State the blood parasite species.
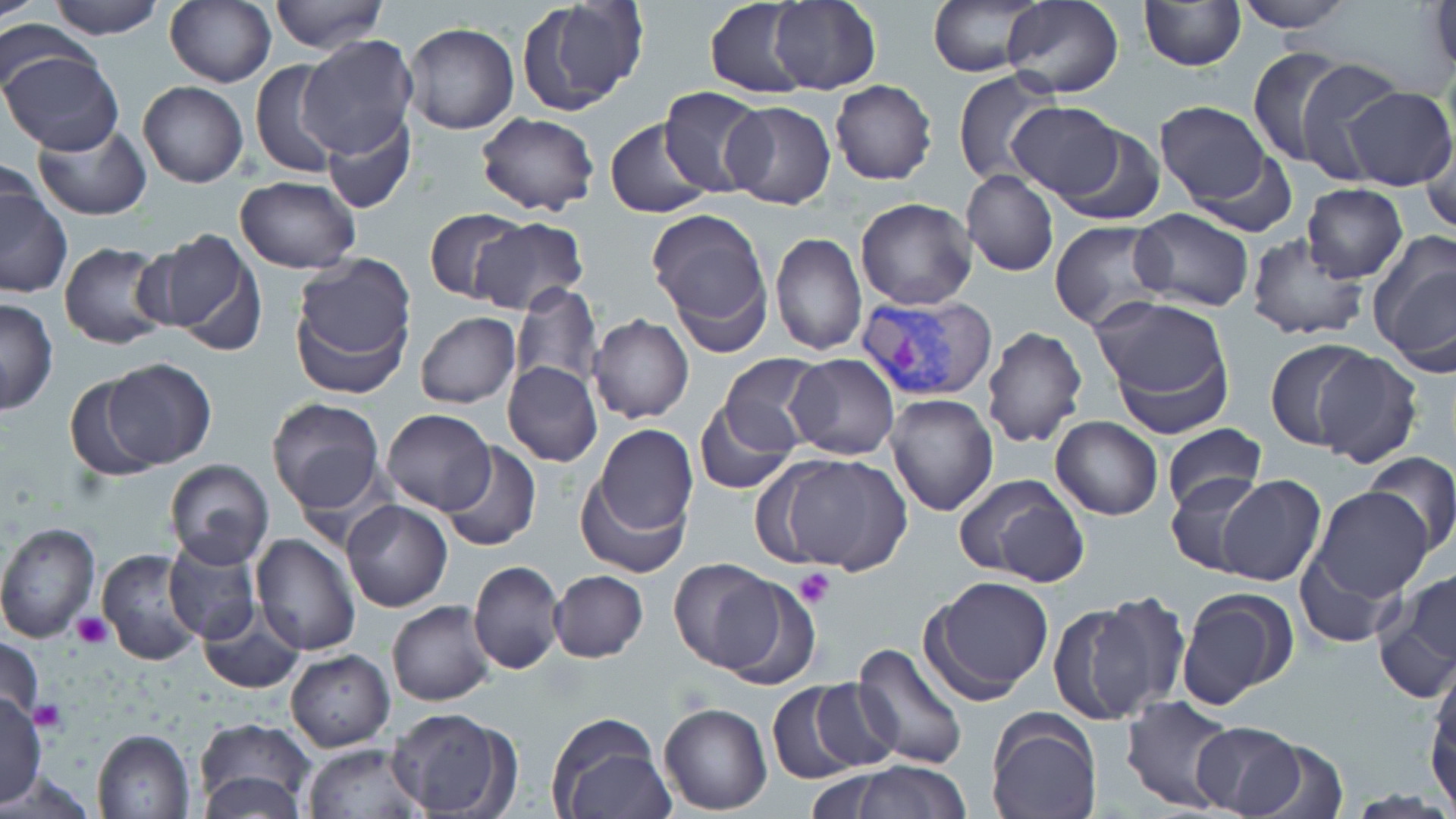
Plasmodium vivax.

preparation = thin blood film
platelet locations = approximate bounding boxes as named x1/y1/x2/y2 corners in pixels: (x1=795, y1=568, x2=835, y2=608), (x1=72, y1=611, x2=113, y2=651), (x1=31, y1=699, x2=65, y2=733)
modality = optical microscopy
image size = 1456×819 pixels
stain = May-Grünwald-Giemsa
Plasmodium vivax-infected red blood cell locations = approximate bounding boxes as named x1/y1/x2/y2 corners in pixels: (x1=855, y1=290, x2=998, y2=399)
field of view = one of a larger specimen
uninfected red blood cell locations = approximate bounding boxes as named x1/y1/x2/y2 corners in pixels: (x1=0, y1=0, x2=39, y2=22), (x1=48, y1=0, x2=165, y2=40), (x1=166, y1=0, x2=277, y2=87), (x1=268, y1=0, x2=387, y2=53), (x1=926, y1=0, x2=1047, y2=77), (x1=1232, y1=0, x2=1355, y2=32), (x1=516, y1=1, x2=649, y2=114), (x1=704, y1=1, x2=814, y2=98), (x1=768, y1=1, x2=881, y2=92), (x1=1002, y1=1, x2=1125, y2=98), (x1=1139, y1=1, x2=1247, y2=71), (x1=1425, y1=1, x2=1455, y2=83), (x1=0, y1=21, x2=89, y2=103), (x1=404, y1=22, x2=519, y2=135), (x1=297, y1=34, x2=418, y2=160), (x1=1246, y1=46, x2=1355, y2=168), (x1=1, y1=48, x2=123, y2=155), (x1=250, y1=59, x2=346, y2=176), (x1=1293, y1=60, x2=1408, y2=184), (x1=953, y1=71, x2=1062, y2=186), (x1=137, y1=80, x2=248, y2=187), (x1=830, y1=80, x2=937, y2=185), (x1=657, y1=86, x2=766, y2=196), (x1=1338, y1=86, x2=1455, y2=191), (x1=721, y1=100, x2=836, y2=209), (x1=1007, y1=101, x2=1124, y2=201), (x1=1154, y1=101, x2=1274, y2=207), (x1=476, y1=110, x2=599, y2=216), (x1=318, y1=111, x2=416, y2=216), (x1=603, y1=118, x2=712, y2=219), (x1=34, y1=122, x2=151, y2=222), (x1=1051, y1=126, x2=1166, y2=225), (x1=1418, y1=126, x2=1456, y2=238), (x1=1188, y1=151, x2=1302, y2=239), (x1=961, y1=169, x2=1059, y2=276), (x1=235, y1=175, x2=360, y2=272), (x1=0, y1=177, x2=72, y2=299), (x1=1302, y1=184, x2=1409, y2=283), (x1=855, y1=198, x2=977, y2=310), (x1=1128, y1=207, x2=1253, y2=311), (x1=648, y1=208, x2=774, y2=348), (x1=424, y1=209, x2=527, y2=304), (x1=469, y1=216, x2=589, y2=314), (x1=1050, y1=220, x2=1171, y2=333), (x1=144, y1=227, x2=265, y2=354), (x1=769, y1=231, x2=866, y2=356), (x1=1244, y1=234, x2=1369, y2=342), (x1=1367, y1=235, x2=1455, y2=374), (x1=57, y1=241, x2=176, y2=349), (x1=290, y1=255, x2=416, y2=396), (x1=510, y1=283, x2=604, y2=391), (x1=1096, y1=294, x2=1235, y2=434), (x1=0, y1=297, x2=58, y2=414), (x1=416, y1=313, x2=521, y2=408), (x1=588, y1=314, x2=694, y2=424), (x1=982, y1=325, x2=1089, y2=449), (x1=1264, y1=340, x2=1372, y2=450), (x1=1309, y1=346, x2=1422, y2=467), (x1=786, y1=354, x2=899, y2=459), (x1=718, y1=355, x2=824, y2=455), (x1=99, y1=358, x2=218, y2=469), (x1=502, y1=361, x2=602, y2=467), (x1=64, y1=377, x2=164, y2=483), (x1=885, y1=392, x2=997, y2=515), (x1=265, y1=397, x2=385, y2=515), (x1=695, y1=398, x2=795, y2=492), (x1=382, y1=408, x2=495, y2=514), (x1=1050, y1=416, x2=1162, y2=521), (x1=1163, y1=422, x2=1267, y2=514), (x1=591, y1=424, x2=698, y2=538), (x1=440, y1=442, x2=541, y2=553), (x1=1362, y1=450, x2=1456, y2=559), (x1=770, y1=452, x2=913, y2=575), (x1=164, y1=459, x2=273, y2=567), (x1=1166, y1=472, x2=1269, y2=576), (x1=575, y1=473, x2=688, y2=577), (x1=954, y1=473, x2=1090, y2=585), (x1=1216, y1=475, x2=1325, y2=587), (x1=1308, y1=487, x2=1434, y2=609), (x1=340, y1=500, x2=453, y2=612), (x1=0, y1=521, x2=100, y2=642), (x1=251, y1=533, x2=360, y2=656), (x1=161, y1=534, x2=263, y2=645), (x1=96, y1=547, x2=207, y2=668), (x1=669, y1=560, x2=787, y2=676), (x1=467, y1=561, x2=566, y2=676), (x1=549, y1=569, x2=649, y2=663), (x1=714, y1=575, x2=822, y2=691), (x1=925, y1=575, x2=1056, y2=702), (x1=1376, y1=579, x2=1456, y2=701), (x1=1177, y1=588, x2=1296, y2=711), (x1=1046, y1=596, x2=1178, y2=725), (x1=387, y1=600, x2=497, y2=707), (x1=198, y1=606, x2=304, y2=694), (x1=0, y1=634, x2=46, y2=732), (x1=849, y1=641, x2=968, y2=769), (x1=285, y1=650, x2=395, y2=752), (x1=1428, y1=659, x2=1456, y2=798), (x1=767, y1=679, x2=883, y2=783), (x1=0, y1=693, x2=48, y2=805), (x1=1119, y1=694, x2=1240, y2=814), (x1=658, y1=701, x2=773, y2=815), (x1=385, y1=707, x2=515, y2=818), (x1=984, y1=709, x2=1103, y2=819), (x1=546, y1=713, x2=673, y2=819), (x1=193, y1=718, x2=317, y2=818), (x1=1190, y1=720, x2=1308, y2=816), (x1=91, y1=729, x2=195, y2=818), (x1=1226, y1=735, x2=1352, y2=819), (x1=301, y1=742, x2=429, y2=819), (x1=843, y1=760, x2=972, y2=818), (x1=196, y1=771, x2=308, y2=818)
magnification = 1000x